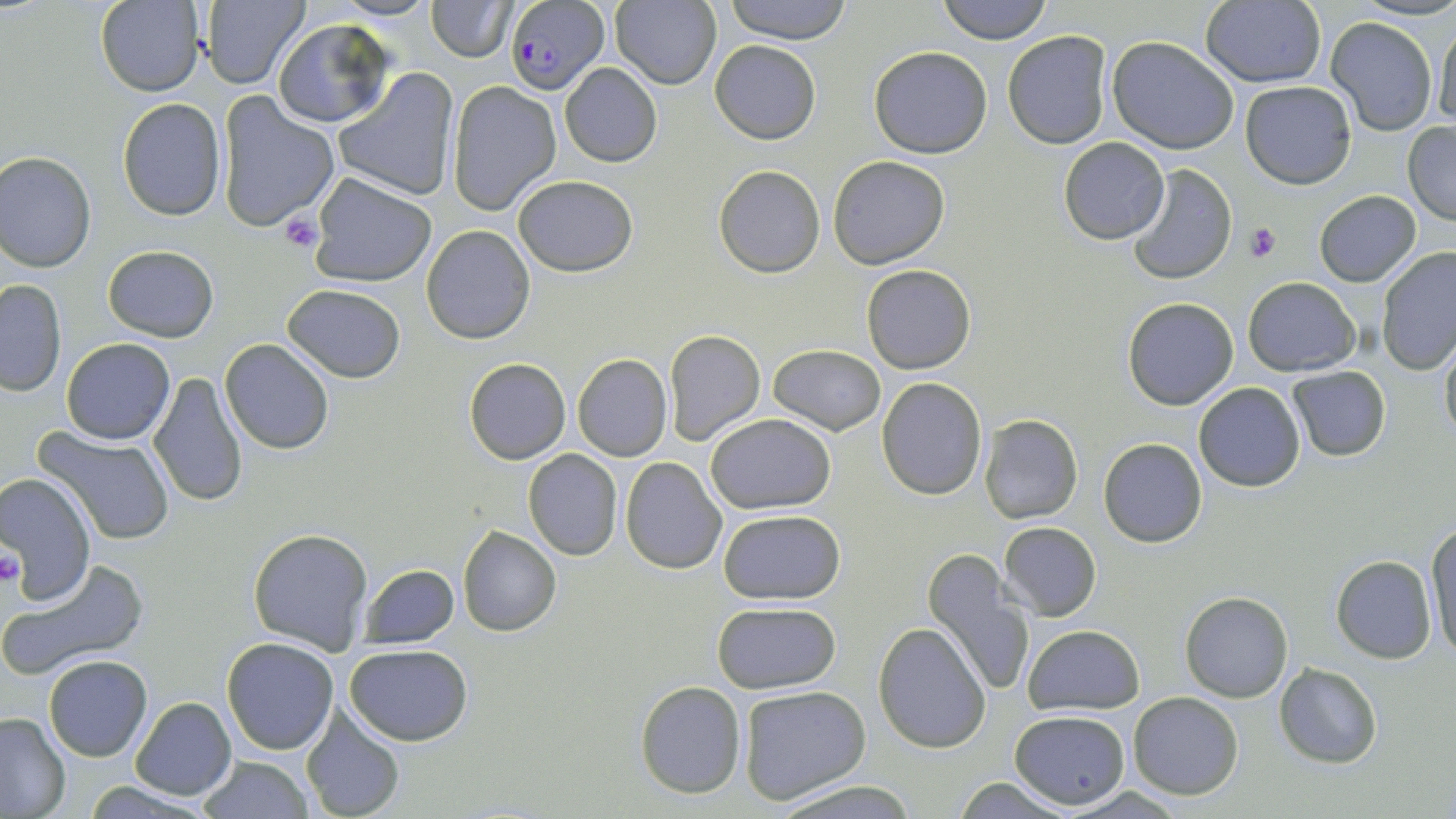
slide_level_diagnosis: Plasmodium falciparum
field_of_view: one of a larger specimen
magnification: 1000x
modality: optical microscopy
uninfected_red_blood_cell_locations: 'approximate bounding boxes as [x1, y1, x2, y2] in pixels: [94, 0, 206, 96], [199, 0, 310, 89], [332, 0, 439, 22], [428, 0, 516, 61], [610, 0, 723, 90], [723, 0, 853, 44], [936, 0, 1053, 44], [1201, 0, 1326, 87], [1324, 16, 1439, 136], [272, 18, 396, 129], [1431, 18, 1454, 126], [1002, 31, 1115, 149], [1107, 36, 1240, 153], [710, 39, 820, 145], [869, 46, 992, 159], [559, 63, 662, 167], [334, 68, 461, 202], [446, 81, 561, 217], [1240, 81, 1357, 188], [217, 93, 340, 235], [116, 98, 227, 221], [1403, 122, 1456, 225], [1058, 138, 1170, 244], [1, 150, 98, 271], [828, 155, 950, 269], [714, 165, 825, 278], [1126, 165, 1236, 285], [308, 173, 437, 287], [512, 175, 638, 275], [1314, 191, 1422, 287], [421, 225, 535, 345], [102, 245, 219, 341], [1377, 248, 1456, 373], [861, 263, 976, 374], [1243, 277, 1360, 377], [0, 279, 66, 395], [282, 284, 406, 382], [1123, 297, 1238, 410], [663, 329, 765, 447], [1439, 334, 1456, 445], [60, 337, 175, 444], [220, 338, 336, 455], [768, 344, 886, 435], [572, 353, 673, 461], [464, 358, 571, 463], [1286, 366, 1391, 462], [149, 370, 248, 508], [877, 377, 988, 500], [1194, 382, 1305, 492], [705, 414, 836, 513], [981, 414, 1083, 524], [34, 426, 177, 544], [1099, 437, 1208, 547], [522, 449, 624, 561], [619, 457, 726, 574], [0, 472, 99, 602], [718, 508, 846, 603], [1424, 521, 1456, 659], [999, 522, 1101, 620], [458, 526, 562, 636], [247, 528, 373, 654], [921, 548, 1034, 697], [1331, 556, 1437, 662], [1, 557, 149, 682], [357, 564, 460, 649], [1179, 591, 1293, 703], [711, 602, 841, 694], [874, 622, 992, 753], [1022, 623, 1145, 714], [223, 637, 339, 755], [344, 643, 473, 745], [43, 654, 152, 761], [1275, 663, 1383, 767], [633, 679, 748, 800], [737, 685, 871, 807], [1128, 692, 1244, 800], [131, 696, 236, 800], [299, 706, 406, 819], [1011, 710, 1130, 809], [0, 711, 72, 817], [199, 755, 314, 819], [948, 777, 1071, 817], [83, 781, 221, 816], [772, 781, 917, 817]'
image_size: 1456×819 pixels
preparation: thin blood smear
stain: May-Grünwald-Giemsa
platelet_locations: 'approximate bounding boxes as [x1, y1, x2, y2] in pixels: [279, 213, 325, 252], [1245, 222, 1281, 263], [0, 550, 25, 587]'
plasmodium_falciparum_infected_red_blood_cell_locations: 'approximate bounding boxes as [x1, y1, x2, y2] in pixels: [507, 0, 609, 93]'